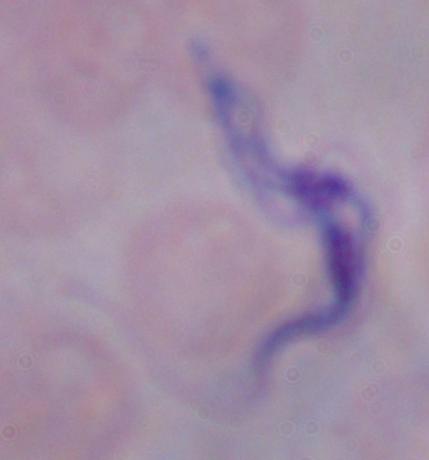
{
  "identification": "trypanosome",
  "modality": "micrograph",
  "magnification": "1000x"
}